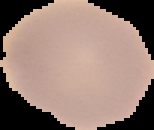

Result: no malaria parasites seen. Segmented cell region on a black background. Image is 154×130 pixels. From a thin blood smear.